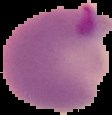
From a thin blood film. Segmented cell region on a black background. Malaria status: parasitized. Image is 112×115 pixels.